Identify the cell.
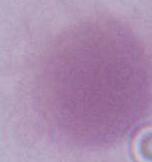
An erythrocyte.

{
  "magnification": "1000x",
  "modality": "micrograph"
}